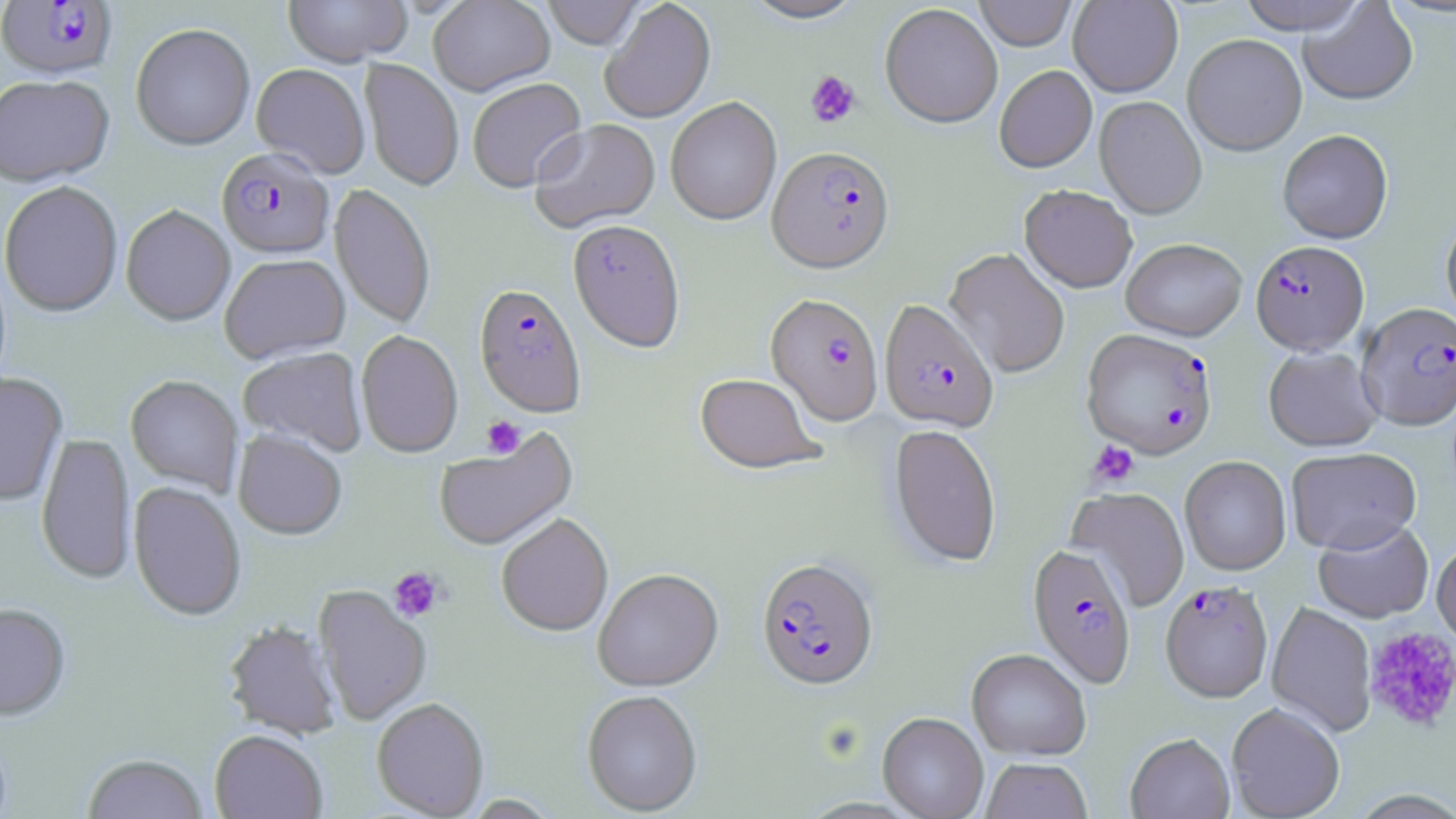 Approximate bounding boxes as (x1,y1)-(x2,y2) corner pairs in pixels. Plasmodium falciparum-infected red blood cell locations: (1,1)-(118,83), (767,148)-(895,273), (216,150)-(335,262), (1251,241)-(1369,354), (474,285)-(587,419), (766,293)-(884,426), (878,299)-(999,434), (1357,302)-(1456,431), (1081,328)-(1218,459), (1027,543)-(1137,688), (756,557)-(879,692), (1160,580)-(1273,703). Uninfected red blood cell locations: (283,0)-(412,69), (428,0)-(555,97), (541,0)-(645,50), (740,0)-(868,24), (974,0)-(1077,51), (1068,0)-(1183,97), (1237,0)-(1370,35), (601,1)-(716,124), (1298,2)-(1418,106), (879,3)-(1003,129), (130,25)-(255,153), (1182,33)-(1308,156), (360,59)-(463,192), (251,65)-(370,179), (994,65)-(1097,173), (362,72)-(574,190), (0,77)-(115,190), (467,79)-(587,194), (1094,96)-(1207,219), (665,97)-(782,226), (530,120)-(661,235), (1277,129)-(1393,244), (1,183)-(123,319), (329,185)-(436,330), (1019,186)-(1138,293), (121,206)-(235,327), (1440,214)-(1456,331), (568,222)-(685,354), (1121,238)-(1247,341), (945,248)-(1070,379), (220,255)-(351,365), (356,331)-(464,458), (1263,346)-(1383,452), (238,348)-(368,456), (0,374)-(68,507), (694,374)-(824,475), (125,375)-(243,496), (889,424)-(1002,568), (433,427)-(578,552), (233,431)-(347,542), (36,433)-(137,586), (1286,446)-(1422,554), (1179,456)-(1291,576), (128,483)-(246,623), (1067,487)-(1190,612), (497,514)-(613,638), (1313,519)-(1435,624), (1431,539)-(1456,651), (593,569)-(723,693), (313,585)-(431,727), (1266,602)-(1377,737), (0,604)-(71,723), (224,622)-(341,741), (966,649)-(1092,761), (582,691)-(703,817), (372,699)-(489,818), (1226,702)-(1345,818), (878,712)-(989,819), (209,731)-(327,819), (1125,733)-(1235,819), (82,754)-(208,819), (981,759)-(1092,819). Platelet locations: (805,70)-(861,129), (482,417)-(526,459), (1087,440)-(1140,489), (389,567)-(444,622), (1362,627)-(1456,733). Slide-level diagnosis: Plasmodium falciparum. Single field of view. Optical microscopy. May-Grünwald-Giemsa-stained preparation. Image is 1456×819 pixels. Captured at 1000x magnification. Thin blood film.